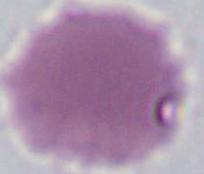
magnification = 1000x
modality = micrograph
identification = red blood cell